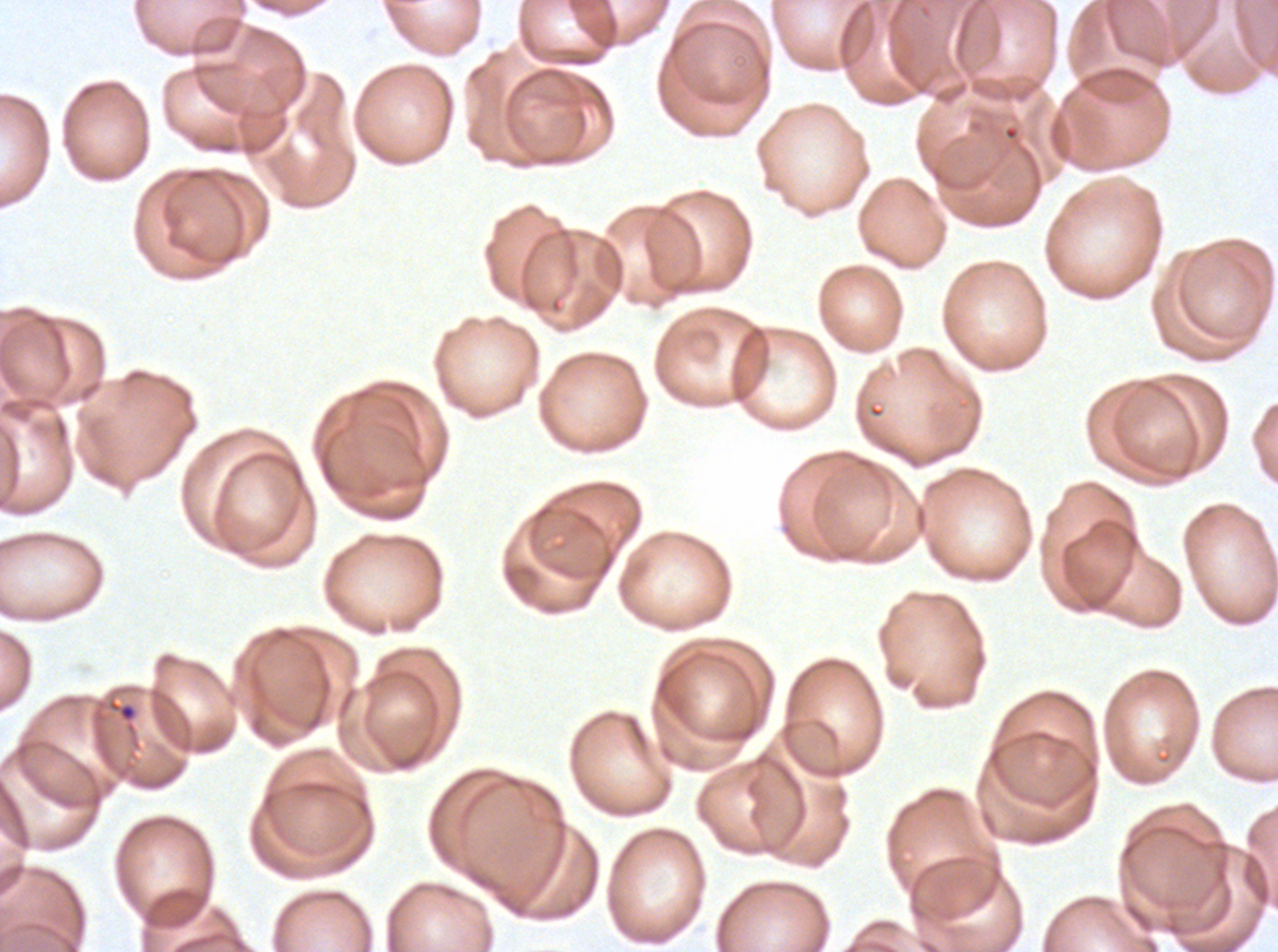
{
  "image_size": "1278×952 pixels",
  "specimen": "P. falciparum from a patient in The Gambia, cultured ex vivo for 24 to 48 hours",
  "field_of_view": "one sub-image of a larger composite",
  "stain": "Giemsa",
  "debris_locations": "approximate bounding boxes as {x1, y1, x2, y2} in pixels: {105, 697, 140, 735}",
  "preparation": "thin blood smear"
}